Locate and identify every blood parasite.
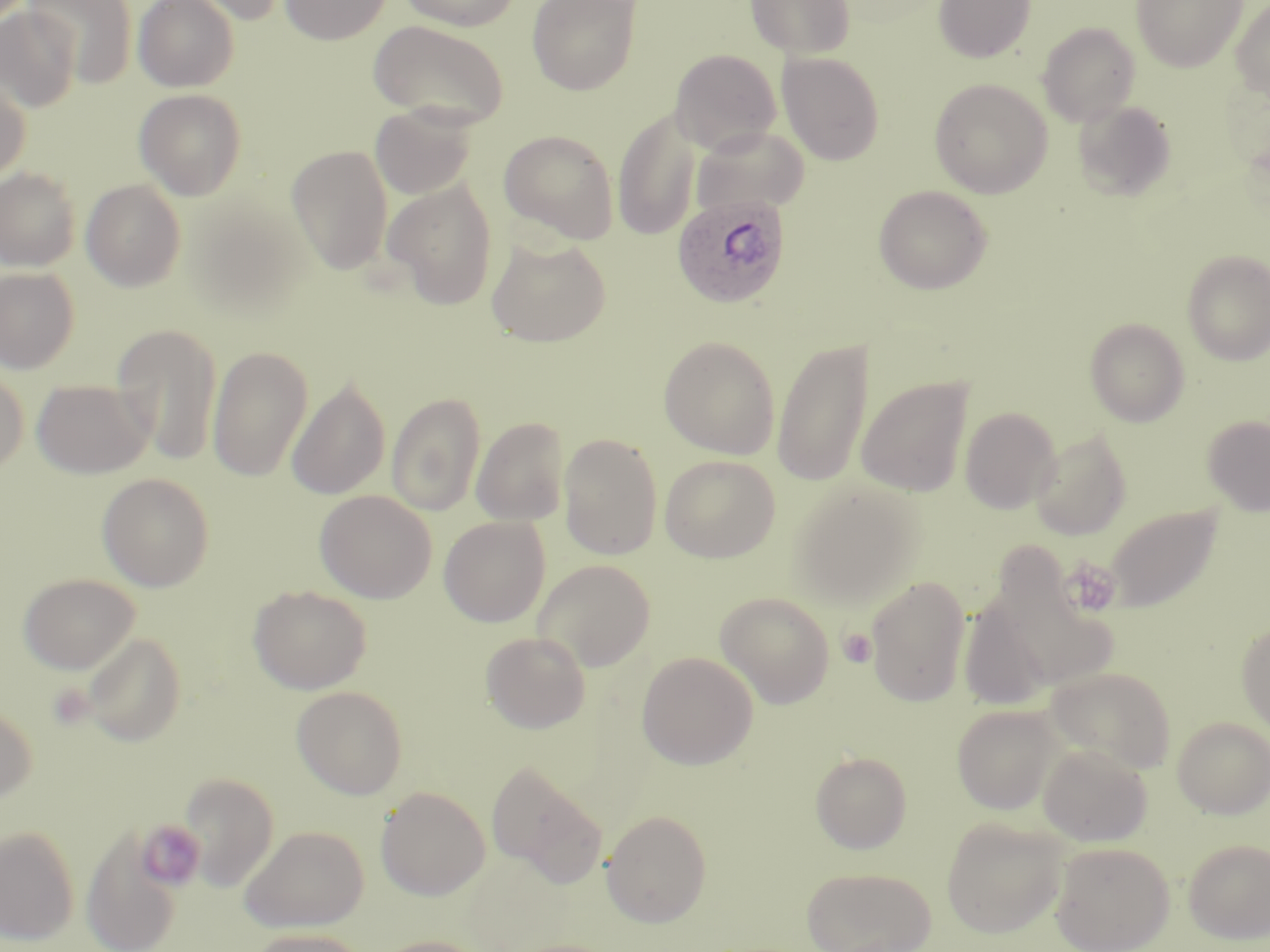
Approximate bounding boxes as (x1, y1, x2, y2) in pixels.
Plasmodium ovale-infected red blood cells: (672, 193, 791, 309).
No Plasmodium falciparum, Plasmodium malariae, Plasmodium vivax, Babesia divergens, or Trypanosoma brucei observed.

Summary:
  - Platelet locations: (1064, 559, 1122, 617), (838, 629, 876, 668), (45, 682, 96, 730), (137, 819, 207, 892)
  - Uninfected red blood cell locations: (25, 0, 138, 87), (133, 0, 238, 92), (176, 0, 294, 26), (280, 0, 392, 45), (397, 0, 522, 31), (526, 0, 643, 96), (744, 0, 856, 60), (933, 0, 1036, 63), (1132, 0, 1247, 72), (1231, 0, 1270, 101), (0, 6, 82, 113), (368, 20, 509, 128), (1036, 22, 1141, 126), (670, 49, 781, 154), (777, 52, 885, 165), (0, 75, 31, 183), (929, 78, 1053, 198), (134, 88, 246, 200), (1072, 99, 1177, 201), (371, 104, 476, 200), (613, 106, 703, 240), (690, 124, 810, 216), (499, 129, 620, 244), (286, 145, 393, 274), (0, 166, 82, 272), (81, 178, 187, 292), (383, 178, 499, 310), (873, 185, 992, 294), (190, 201, 311, 319), (486, 235, 611, 347), (1182, 249, 1270, 365), (0, 267, 79, 373), (1084, 317, 1190, 426), (112, 323, 223, 466), (658, 335, 780, 459), (773, 336, 872, 488), (207, 345, 313, 481), (0, 367, 29, 476), (857, 376, 973, 497), (287, 377, 390, 500), (32, 379, 152, 478), (386, 391, 485, 517), (959, 407, 1061, 513), (1201, 415, 1270, 516), (471, 416, 570, 526), (1029, 430, 1132, 540), (559, 433, 663, 560), (659, 454, 780, 563), (97, 472, 215, 592), (788, 480, 924, 607), (314, 490, 437, 603), (1106, 504, 1222, 613), (439, 515, 550, 627), (980, 558, 1122, 698), (533, 559, 655, 671), (16, 573, 140, 674), (864, 574, 972, 707), (247, 584, 372, 694), (715, 592, 835, 709), (959, 595, 1054, 713), (1236, 620, 1270, 737), (481, 631, 591, 733), (79, 632, 186, 747), (636, 651, 759, 770), (1044, 665, 1177, 774), (291, 685, 408, 799), (0, 702, 37, 806), (952, 704, 1064, 814), (1172, 716, 1270, 818), (1038, 743, 1153, 846), (810, 751, 912, 853), (485, 758, 607, 888), (180, 772, 278, 890), (375, 786, 491, 901), (602, 809, 712, 928), (940, 817, 1067, 938), (239, 824, 369, 932), (0, 825, 80, 946), (81, 828, 183, 952), (1183, 838, 1270, 944), (1049, 840, 1175, 951), (800, 865, 937, 952), (244, 927, 371, 952), (371, 935, 490, 952)
  - Slide-level diagnosis: Plasmodium ovale
  - Magnification: 1000x
  - Stain: May-Grünwald-Giemsa
  - Modality: light microscopy
  - Field of view: single
  - Image size: 1270×952 pixels
  - Preparation: thin blood smear